Locate every blood parasite and identify its species.
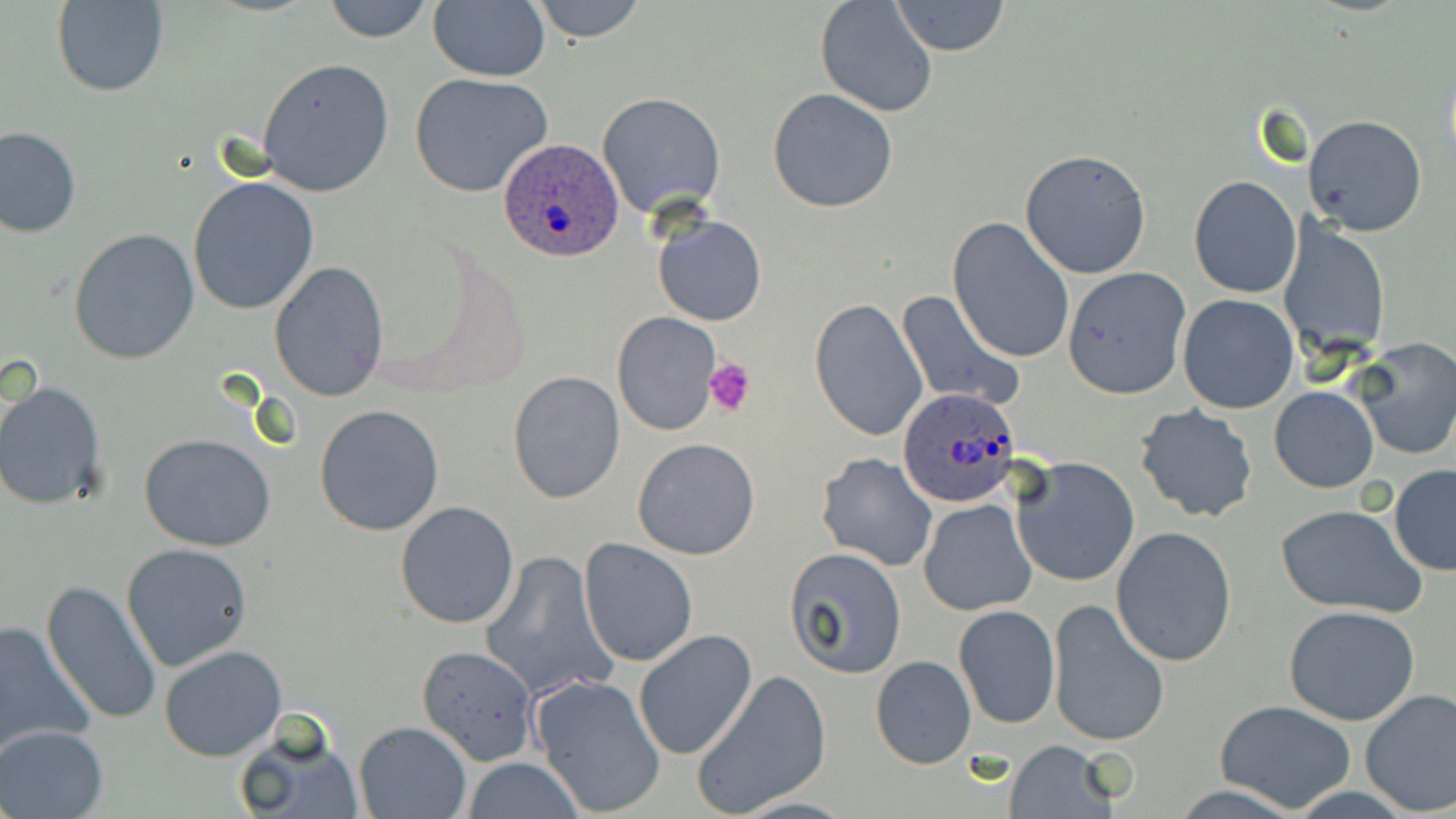
Approximate bounding boxes as named x1/y1/x2/y2 corners in pixels.
Plasmodium ovale-infected red blood cells: (x1=500, y1=138, x2=626, y2=261), (x1=897, y1=386, x2=1022, y2=508).
No Plasmodium falciparum, Plasmodium malariae, Plasmodium vivax, Babesia divergens, or Trypanosoma brucei observed.

Summary:
  - Uninfected red blood cell locations: (x1=323, y1=0, x2=435, y2=43), (x1=528, y1=0, x2=648, y2=44), (x1=51, y1=1, x2=168, y2=98), (x1=814, y1=1, x2=939, y2=119), (x1=891, y1=1, x2=1009, y2=56), (x1=427, y1=2, x2=550, y2=82), (x1=256, y1=58, x2=395, y2=196), (x1=409, y1=73, x2=554, y2=197), (x1=767, y1=87, x2=898, y2=214), (x1=598, y1=92, x2=726, y2=218), (x1=1304, y1=114, x2=1428, y2=237), (x1=0, y1=126, x2=81, y2=238), (x1=1020, y1=149, x2=1152, y2=279), (x1=1189, y1=175, x2=1301, y2=297), (x1=187, y1=177, x2=320, y2=315), (x1=652, y1=214, x2=766, y2=326), (x1=948, y1=216, x2=1076, y2=365), (x1=1281, y1=223, x2=1392, y2=357), (x1=68, y1=228, x2=201, y2=365), (x1=270, y1=261, x2=390, y2=401), (x1=1062, y1=266, x2=1191, y2=399), (x1=897, y1=291, x2=1025, y2=412), (x1=1178, y1=294, x2=1299, y2=414), (x1=809, y1=298, x2=928, y2=441), (x1=612, y1=312, x2=719, y2=435), (x1=1347, y1=337, x2=1456, y2=462), (x1=507, y1=371, x2=627, y2=505), (x1=0, y1=381, x2=107, y2=509), (x1=1269, y1=386, x2=1378, y2=493), (x1=314, y1=404, x2=445, y2=537), (x1=1134, y1=404, x2=1258, y2=524), (x1=139, y1=433, x2=276, y2=552), (x1=633, y1=437, x2=761, y2=559), (x1=816, y1=453, x2=938, y2=572), (x1=1012, y1=455, x2=1139, y2=586), (x1=1389, y1=465, x2=1456, y2=576), (x1=918, y1=499, x2=1037, y2=617), (x1=395, y1=500, x2=521, y2=630), (x1=1275, y1=501, x2=1429, y2=617), (x1=1111, y1=526, x2=1237, y2=667), (x1=578, y1=538, x2=700, y2=666), (x1=121, y1=543, x2=254, y2=671), (x1=783, y1=546, x2=907, y2=677), (x1=479, y1=550, x2=613, y2=701), (x1=40, y1=580, x2=163, y2=727), (x1=1046, y1=598, x2=1169, y2=745), (x1=1284, y1=604, x2=1420, y2=725), (x1=954, y1=605, x2=1059, y2=729), (x1=0, y1=616, x2=96, y2=758), (x1=634, y1=628, x2=758, y2=761), (x1=1316, y1=641, x2=1456, y2=796), (x1=160, y1=644, x2=288, y2=762), (x1=417, y1=645, x2=539, y2=765), (x1=869, y1=655, x2=976, y2=769), (x1=691, y1=670, x2=832, y2=817), (x1=529, y1=673, x2=666, y2=815), (x1=1360, y1=688, x2=1456, y2=816), (x1=1214, y1=700, x2=1358, y2=812), (x1=352, y1=720, x2=473, y2=818), (x1=1, y1=724, x2=108, y2=818), (x1=234, y1=724, x2=364, y2=819), (x1=1003, y1=738, x2=1120, y2=817), (x1=460, y1=758, x2=585, y2=817)
  - Platelet locations: (x1=703, y1=356, x2=757, y2=417)
  - Slide-level diagnosis: Plasmodium ovale
  - Magnification: 1000x
  - Preparation: thin blood film
  - Image size: 1456×819 pixels
  - Stain: May-Grünwald-Giemsa
  - Modality: optical microscopy
  - Field of view: one of a larger specimen